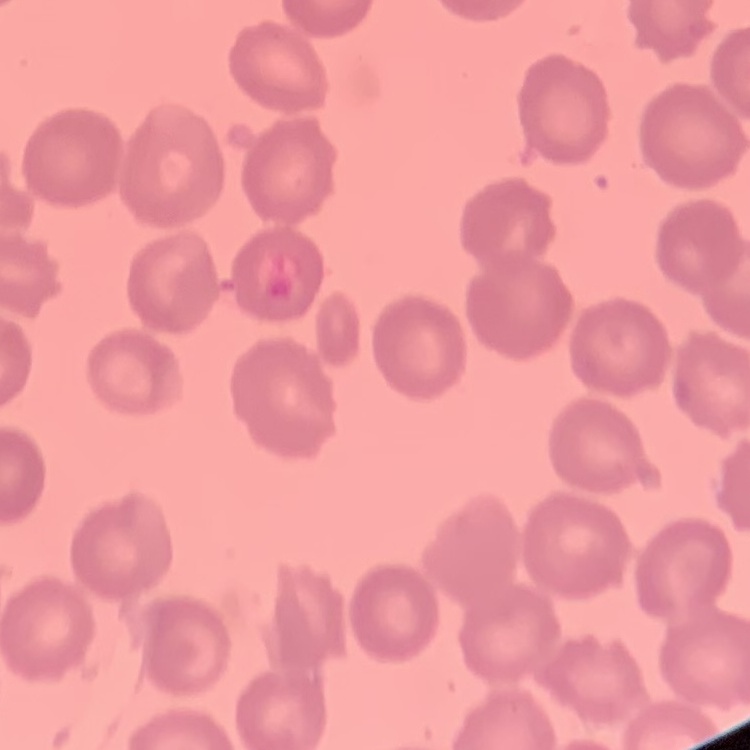

Summary:
  - Erythrocyte morphology: no rouleaux formation
  - Image type: square crop of a larger photomicrograph
  - Preparation: thin blood smear
  - Stain: Field's or Giemsa